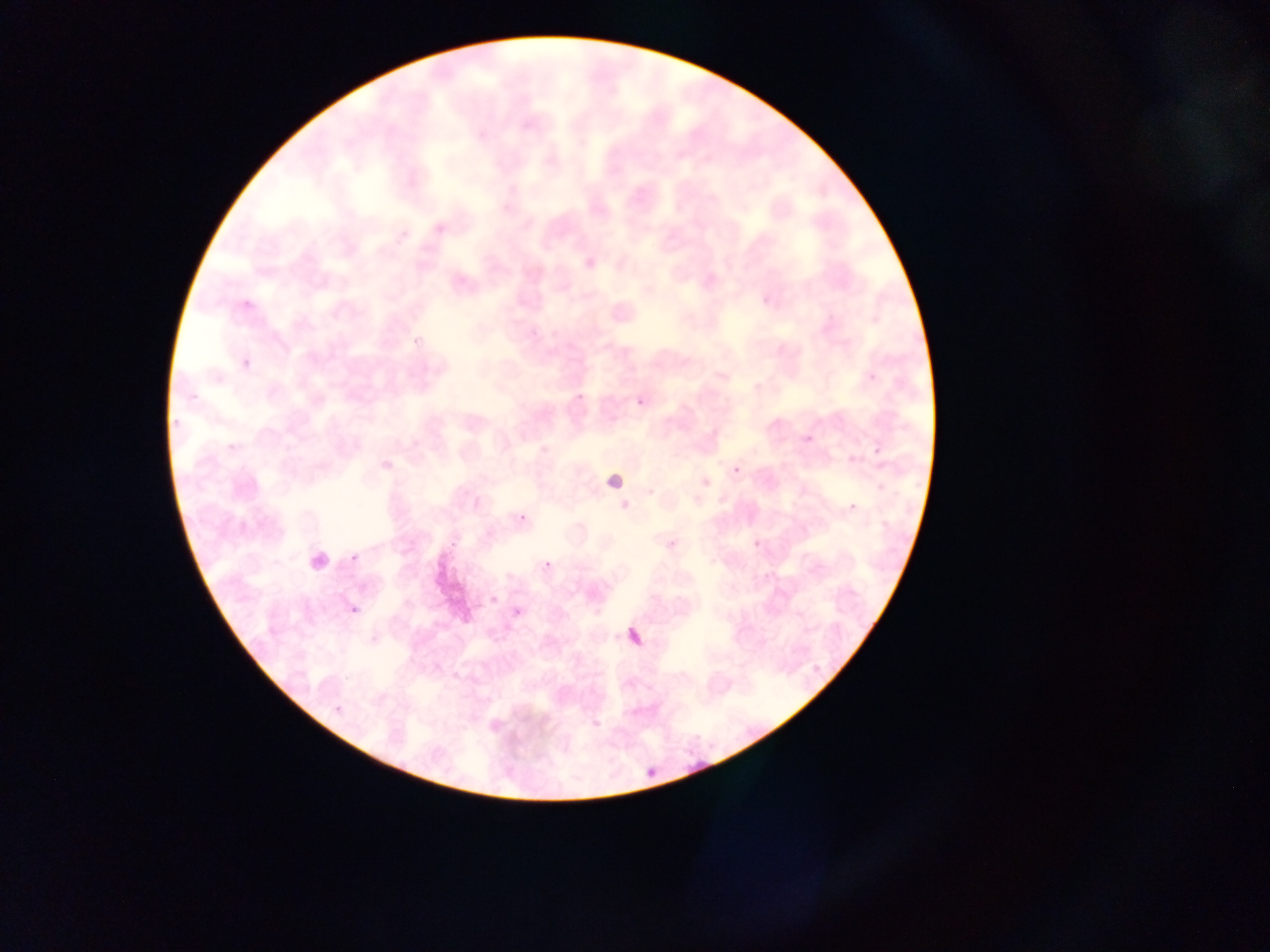
Approximate bounding boxes as left top right bottom in pixels.
Summary:
  - Malaria parasite locations: 242 357 254 378; 633 393 646 407; 575 394 589 408; 799 425 822 448; 871 449 880 457; 843 452 859 469; 733 466 741 474; 845 504 855 517; 518 513 527 522; 448 541 468 561; 346 554 362 566; 542 556 561 573; 490 594 500 605; 345 602 365 625; 628 626 650 659; 680 752 703 773; 642 759 657 792
  - Preparation: thin blood smear
  - Image size: 1270×952 pixels
  - Country: Ghana
  - Field of view: single
  - Capture: mobile-phone photograph through a microscope